Identify the parasite.
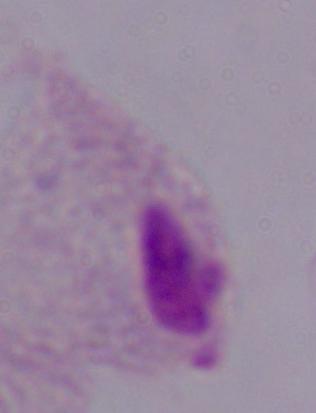

A trichomonad.

Photomicrograph. Captured at 1000x magnification.